Describe the morphology of the erythrocytes.
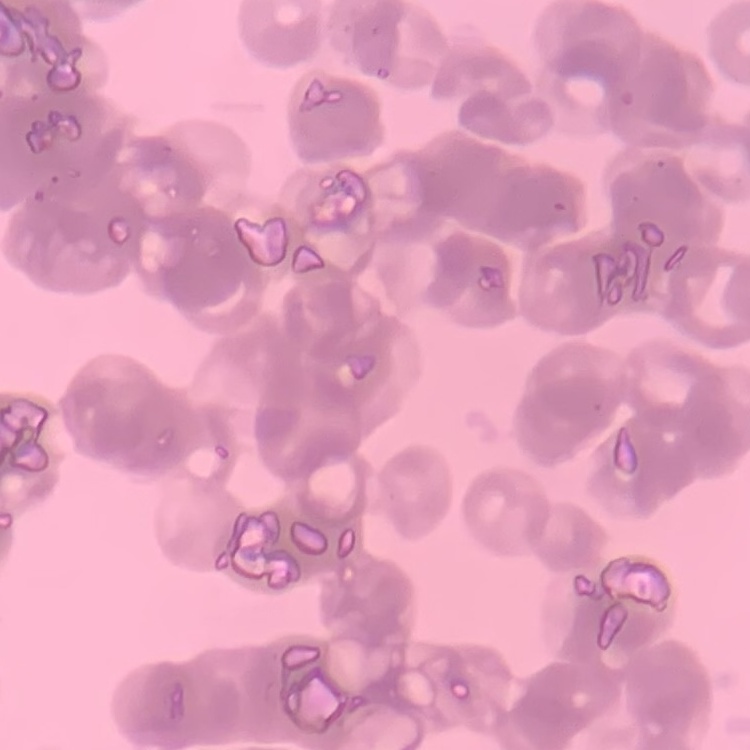
They show rouleaux formation.

preparation = thin blood film
image type = square crop of a larger photomicrograph
stain = Field's or Giemsa